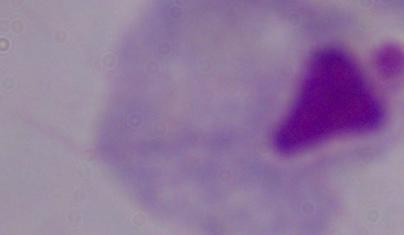

magnification: 1000x
modality: photomicrograph
identification: trichomonad